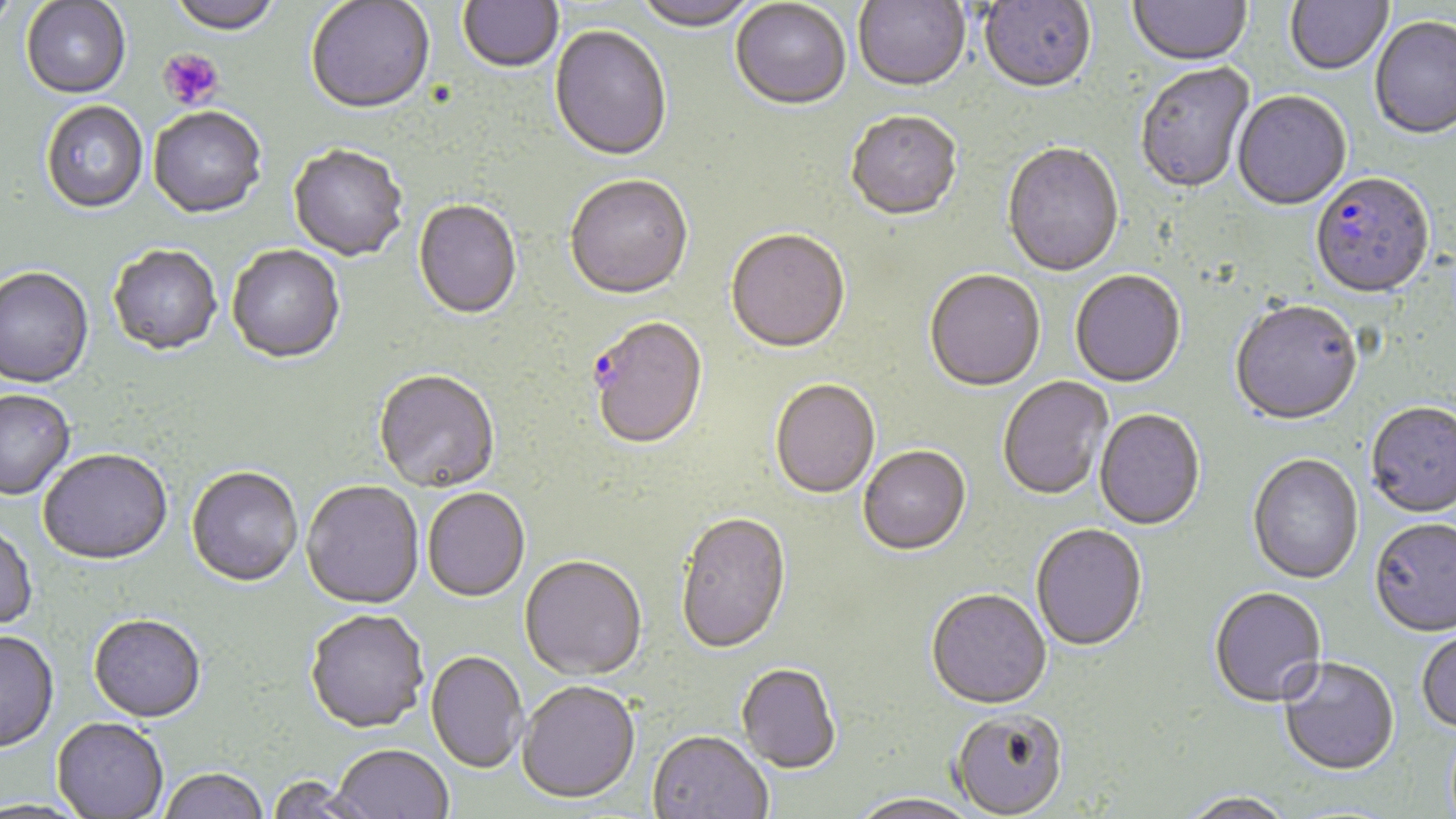

slide-level diagnosis = Plasmodium falciparum
image size = 1456×819 pixels
field of view = single
preparation = thin blood film
stain = May-Grünwald-Giemsa
platelet locations = approximate bounding boxes as (x1,y1)-(x2,y2) corner pairs in pixels: (158,49)-(224,110)
magnification = 1000x
uninfected red blood cell locations = approximate bounding boxes as (x1,y1)-(x2,y2) corner pairs in pixels: (0,0)-(21,33), (167,0)-(281,38), (458,0)-(563,75), (634,0)-(757,34), (853,0)-(971,95), (979,0)-(1097,97), (1129,0)-(1252,70), (1285,0)-(1393,77), (21,1)-(131,100), (306,1)-(436,118), (730,2)-(851,113), (1369,18)-(1456,142), (549,27)-(672,164), (1136,64)-(1256,196), (1232,93)-(1352,213), (41,102)-(148,216), (148,109)-(266,221), (845,114)-(963,224), (1002,144)-(1124,279), (288,146)-(408,263), (564,177)-(694,303), (413,201)-(522,322), (726,231)-(851,356), (109,246)-(222,358), (227,246)-(346,366), (0,268)-(95,390), (925,271)-(1046,393), (1070,271)-(1186,389), (1230,302)-(1364,428), (373,372)-(500,494), (998,376)-(1114,503), (770,381)-(880,501), (0,392)-(76,502), (1365,404)-(1456,520), (1095,410)-(1205,532), (858,447)-(971,558), (38,451)-(173,568), (1247,455)-(1363,586), (186,469)-(303,590), (301,482)-(425,611), (423,490)-(530,604), (676,514)-(792,658), (1369,521)-(1456,639), (0,525)-(39,633), (1031,525)-(1147,653), (519,558)-(648,683), (1209,589)-(1327,710), (926,591)-(1052,712), (305,612)-(429,736), (88,617)-(206,725), (1416,629)-(1456,735), (0,633)-(60,755), (425,652)-(528,775), (1278,659)-(1399,779), (736,665)-(841,776), (516,684)-(641,807), (950,712)-(1069,819), (51,719)-(168,818), (647,733)-(772,819), (330,746)-(453,819), (159,770)-(267,819), (266,776)-(373,819), (1181,793)-(1296,819), (848,795)-(980,819)
Plasmodium falciparum-infected red blood cell locations = approximate bounding boxes as (x1,y1)-(x2,y2) corner pairs in pixels: (1310,175)-(1435,301), (588,319)-(708,453)
modality = optical microscopy